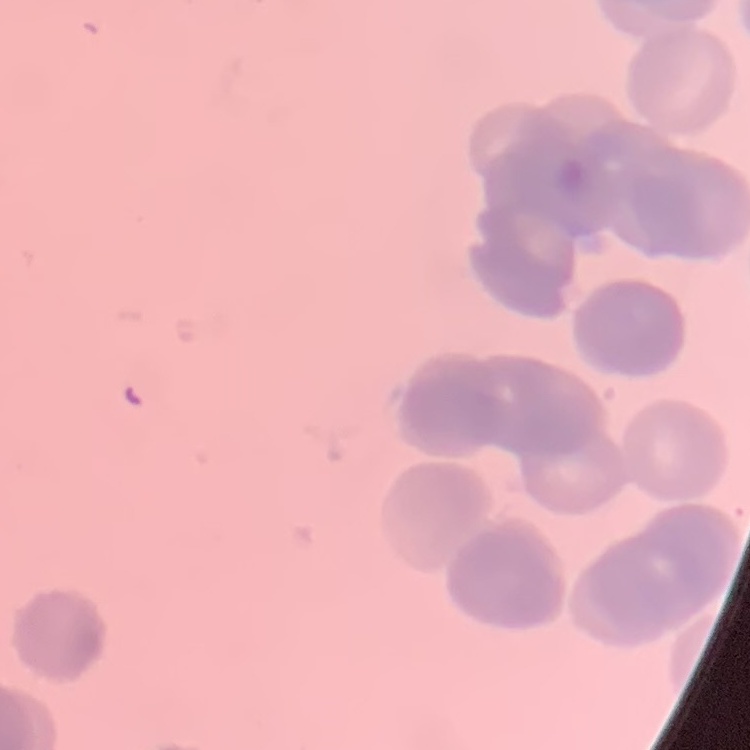
erythrocyte morphology = rouleaux formation
stain = Field's or Giemsa
image type = one tile cut from a larger photomicrograph
preparation = thin blood smear